Classify this cell by malaria status.
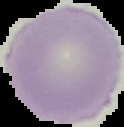
Uninfected.

From a thin blood smear. Image is 124×127 pixels. Segmented cell region on a black background.